Assess this cell for malaria.
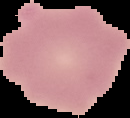
Uninfected.

Image is 130×118 pixels. From a thin blood smear. Segmented cell region on a black background.